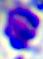 400x magnification. Micrograph. A white blood cell is shown.